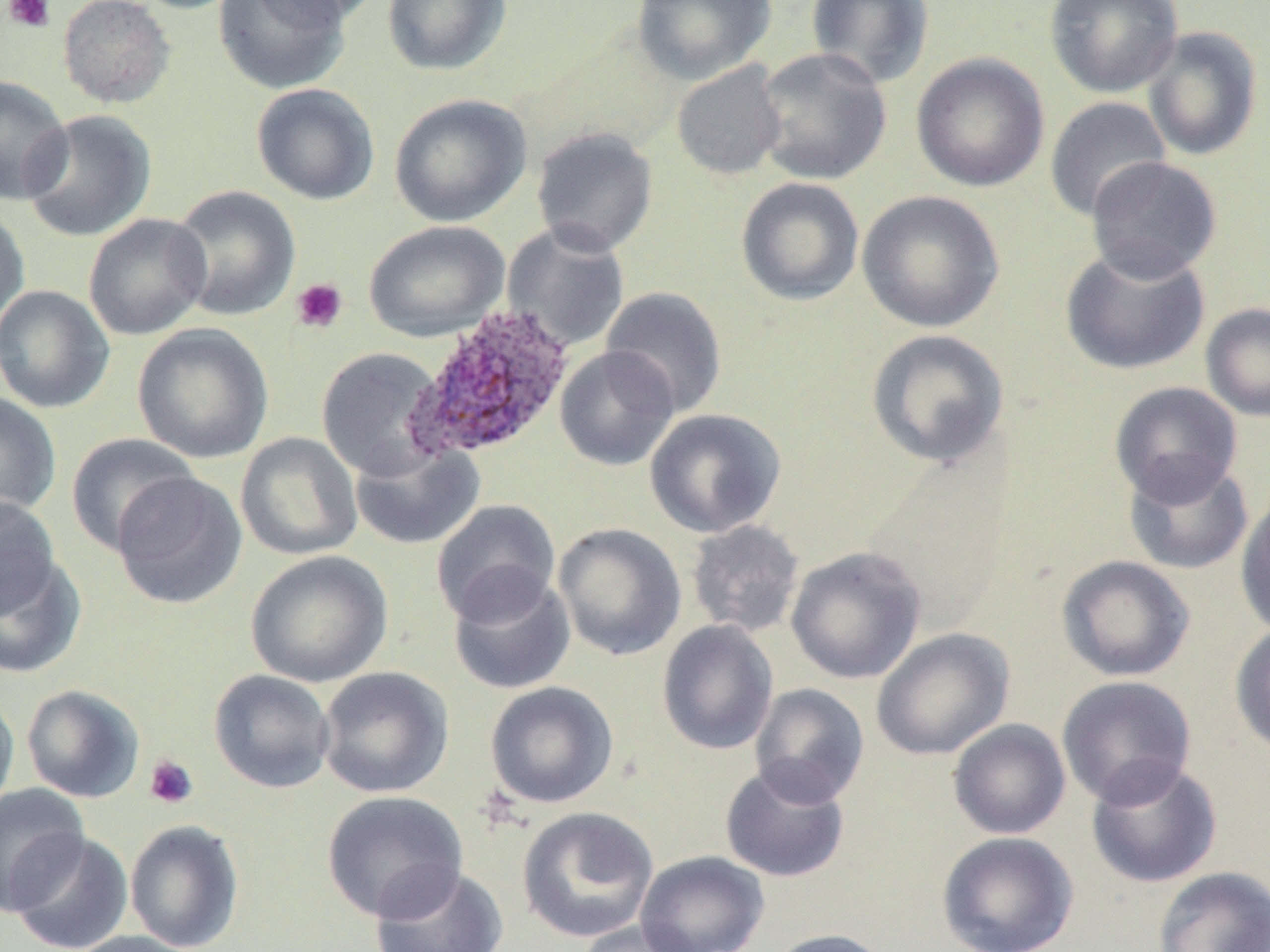

Approximate bounding boxes as [x1, y1, x2, y2] in pixels. Platelet locations: [3, 0, 56, 33], [290, 278, 348, 333], [143, 754, 199, 809]. Plasmodium ovale-infected red blood cell locations: [404, 306, 576, 462]. Uninfected red blood cell locations: [57, 0, 176, 108], [127, 0, 246, 14], [213, 0, 351, 95], [249, 0, 379, 28], [382, 0, 512, 76], [632, 0, 775, 84], [806, 0, 935, 89], [1044, 0, 1183, 98], [1142, 26, 1263, 161], [753, 47, 892, 186], [911, 52, 1049, 193], [671, 61, 787, 180], [0, 76, 73, 203], [250, 83, 380, 205], [389, 93, 532, 227], [1044, 96, 1171, 222], [19, 109, 157, 243], [531, 127, 658, 256], [1085, 156, 1222, 281], [735, 177, 865, 306], [168, 185, 301, 321], [856, 190, 1005, 333], [0, 204, 30, 333], [83, 213, 212, 341], [364, 219, 509, 342], [501, 223, 630, 352], [1060, 243, 1210, 376], [0, 285, 115, 414], [599, 286, 728, 418], [1201, 303, 1270, 422], [132, 323, 274, 463], [865, 329, 1010, 470], [555, 346, 679, 471], [316, 347, 447, 478], [1109, 381, 1243, 505], [0, 391, 61, 521], [644, 408, 787, 538], [66, 432, 198, 556], [235, 432, 363, 560], [349, 440, 485, 550], [1123, 456, 1254, 575], [111, 472, 247, 610], [1235, 488, 1270, 639], [1, 496, 60, 620], [431, 499, 561, 624], [686, 519, 805, 638], [553, 522, 687, 661], [786, 546, 926, 684], [245, 550, 394, 688], [0, 553, 86, 679], [1056, 555, 1196, 682], [447, 569, 576, 695], [657, 620, 778, 755], [1230, 622, 1270, 758], [871, 628, 1014, 760], [317, 666, 454, 798], [208, 669, 335, 794], [1056, 675, 1198, 806], [484, 681, 619, 809], [749, 683, 870, 807], [21, 685, 145, 803], [0, 691, 20, 818], [948, 719, 1071, 840], [1085, 757, 1222, 888], [719, 762, 850, 883], [0, 783, 91, 915], [321, 790, 468, 923], [517, 806, 659, 943], [125, 818, 245, 952], [6, 830, 134, 952], [937, 831, 1079, 952], [636, 850, 769, 952], [370, 864, 509, 952], [1153, 866, 1270, 952], [575, 920, 707, 952], [764, 928, 895, 952], [66, 930, 202, 952]. Slide-level diagnosis: Plasmodium ovale. Captured at 1000x magnification. Thin blood film. Light microscopy. May-Grünwald-Giemsa-stained preparation. Image is 1270×952 pixels. One field of a larger specimen.